Locate and identify every blood parasite.
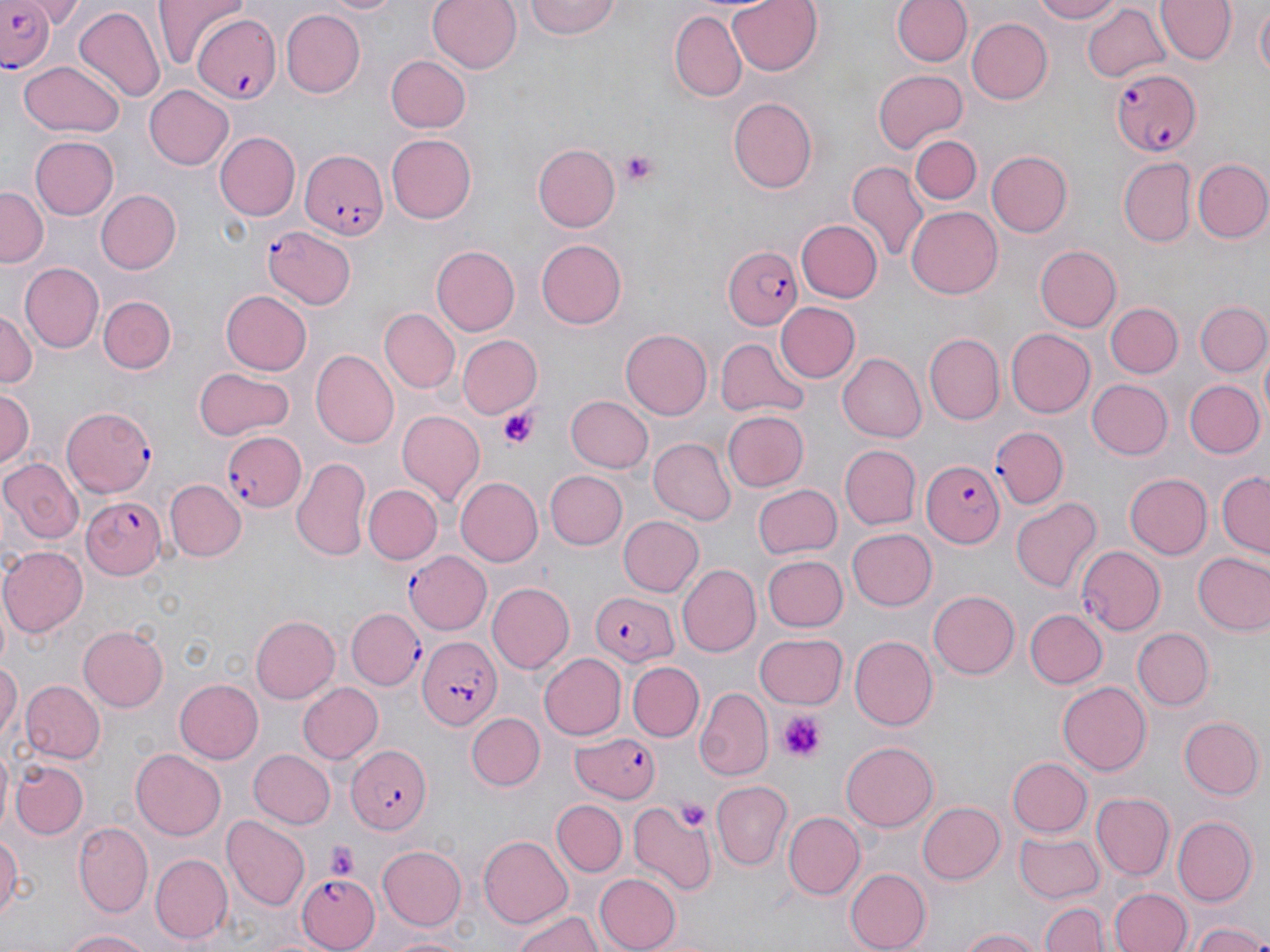

Approximate bounding boxes as [x1, y1, x2, y2] in pixels.
Plasmodium falciparum-infected red blood cells (subset): [0, 3, 58, 73], [191, 15, 279, 102], [1109, 67, 1202, 158], [299, 149, 386, 242], [263, 226, 357, 311], [722, 243, 806, 332], [63, 404, 152, 494], [991, 425, 1068, 509], [222, 429, 305, 513], [919, 461, 1004, 549], [83, 495, 165, 578], [589, 589, 681, 663], [418, 638, 498, 730], [344, 744, 432, 836], [297, 873, 377, 950].
No Plasmodium ovale, Plasmodium malariae, Plasmodium vivax, Babesia divergens, or Trypanosoma brucei observed.

Platelet locations: [621, 150, 660, 187], [497, 408, 540, 449], [780, 713, 823, 760], [676, 798, 710, 828], [323, 841, 361, 879]. Uninfected red blood cell locations (subset): [155, 0, 246, 68], [315, 0, 405, 17], [426, 0, 522, 75], [523, 0, 621, 40], [725, 0, 821, 75], [892, 0, 972, 68], [1026, 0, 1124, 24], [1155, 0, 1235, 65], [1080, 3, 1174, 83], [1252, 4, 1269, 85], [73, 7, 166, 103], [280, 9, 364, 98], [670, 11, 746, 103], [965, 16, 1052, 103], [408, 23, 505, 127], [385, 56, 472, 134], [17, 61, 124, 138], [873, 70, 967, 151], [143, 84, 232, 170], [727, 95, 816, 193], [216, 132, 299, 219], [909, 132, 983, 206], [386, 134, 477, 223], [30, 137, 119, 220], [533, 144, 621, 230], [986, 152, 1072, 236], [1119, 158, 1196, 247], [1192, 158, 1270, 244], [847, 163, 926, 264], [0, 186, 47, 267], [94, 189, 180, 274], [907, 206, 1002, 298], [793, 218, 883, 304], [534, 239, 626, 330], [432, 245, 521, 335], [1036, 245, 1122, 331], [18, 261, 102, 353], [220, 290, 311, 376], [98, 296, 175, 374], [1195, 299, 1268, 378], [774, 301, 860, 384], [1107, 304, 1182, 377], [0, 308, 39, 390], [380, 309, 460, 393], [1008, 327, 1096, 418], [621, 328, 715, 419], [924, 333, 1005, 423], [455, 334, 542, 420], [714, 338, 811, 421], [312, 349, 398, 446], [837, 353, 926, 441], [195, 366, 295, 438], [1088, 379, 1174, 459], [1185, 380, 1263, 457], [1, 385, 37, 469], [566, 395, 653, 472], [397, 411, 485, 504], [722, 411, 810, 491], [648, 437, 736, 524], [838, 445, 921, 530], [292, 456, 371, 562], [4, 458, 83, 545], [545, 470, 628, 550], [1217, 470, 1269, 558], [1123, 473, 1213, 560], [454, 476, 544, 568], [166, 479, 243, 560], [751, 483, 842, 560], [363, 484, 442, 564], [1011, 496, 1102, 595], [617, 515, 703, 598], [848, 528, 936, 612], [1076, 546, 1166, 634], [1, 547, 87, 636], [1191, 549, 1270, 636], [405, 550, 493, 635], [765, 555, 848, 632], [679, 566, 760, 655], [486, 582, 574, 674], [929, 588, 1020, 677], [348, 606, 423, 689], [1026, 610, 1107, 689], [249, 615, 339, 704], [78, 625, 170, 709], [1134, 629, 1213, 708], [755, 633, 848, 709], [851, 635, 937, 729], [538, 653, 626, 738], [0, 656, 21, 746], [627, 661, 705, 740], [18, 679, 104, 764], [174, 679, 263, 765], [1056, 679, 1150, 772], [297, 681, 383, 765], [695, 689, 770, 780], [467, 712, 544, 791], [1179, 716, 1263, 799], [839, 739, 937, 831], [131, 749, 227, 838], [247, 749, 336, 828], [1009, 757, 1093, 837], [11, 760, 88, 838], [712, 780, 793, 868], [1092, 792, 1175, 881], [551, 799, 627, 876], [628, 799, 719, 894], [916, 800, 1004, 884], [783, 810, 865, 899], [221, 813, 310, 908], [1173, 817, 1257, 904], [74, 821, 152, 915], [0, 828, 22, 925], [1013, 831, 1105, 901], [478, 835, 573, 928], [377, 844, 467, 932], [152, 853, 233, 942], [842, 865, 929, 952], [596, 872, 683, 952], [1109, 888, 1191, 952], [1041, 899, 1107, 952], [511, 908, 607, 952], [1189, 921, 1270, 952], [955, 927, 1043, 952], [58, 928, 157, 952], [381, 931, 471, 952]. Slide-level diagnosis: Plasmodium falciparum. Light microscopy. One field of a larger specimen. May-Grünwald-Giemsa-stained preparation. Image is 1270×952 pixels. 1000x magnification. Thin blood smear.